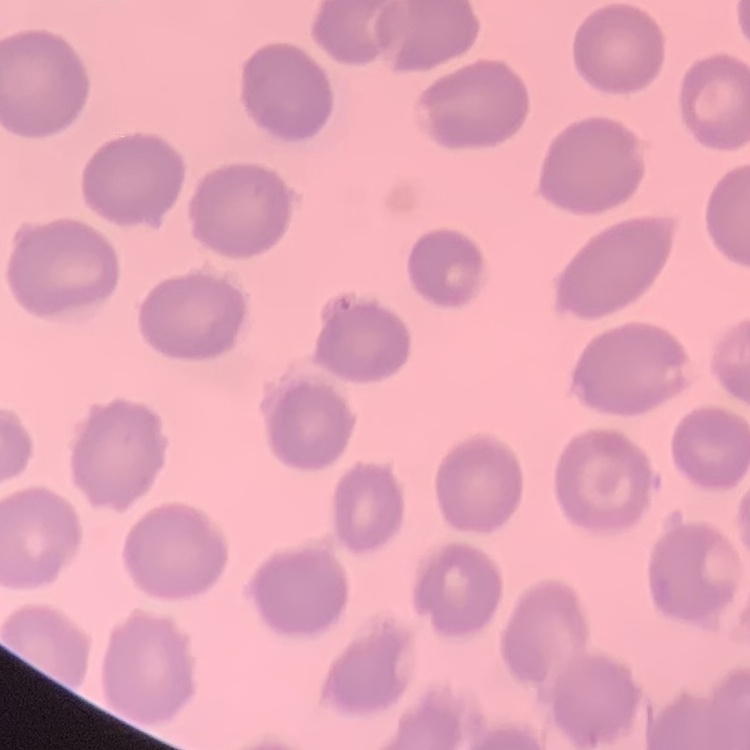

Summary:
  - Erythrocyte morphology: no rouleaux formation
  - Preparation: thin blood smear
  - Stain: Field's or Giemsa
  - Image type: one tile cut from a larger photomicrograph